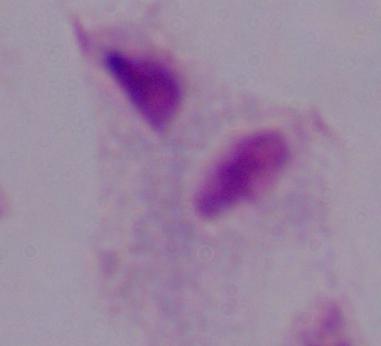
Summary:
  - Modality: photomicrograph
  - Identification: trichomonad
  - Magnification: 1000x